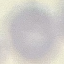
result = no malaria parasites detected
preparation = thin smear
image type = automatically extracted cell patch, resized to 64 × 64 pixels
capture = smartphone camera at the microscope eyepiece
stain = Giemsa